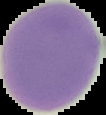 Result: no malaria parasites detected. Image is 106×115 pixels. The area outside the segmented cell region is set to black. From a thin blood film.